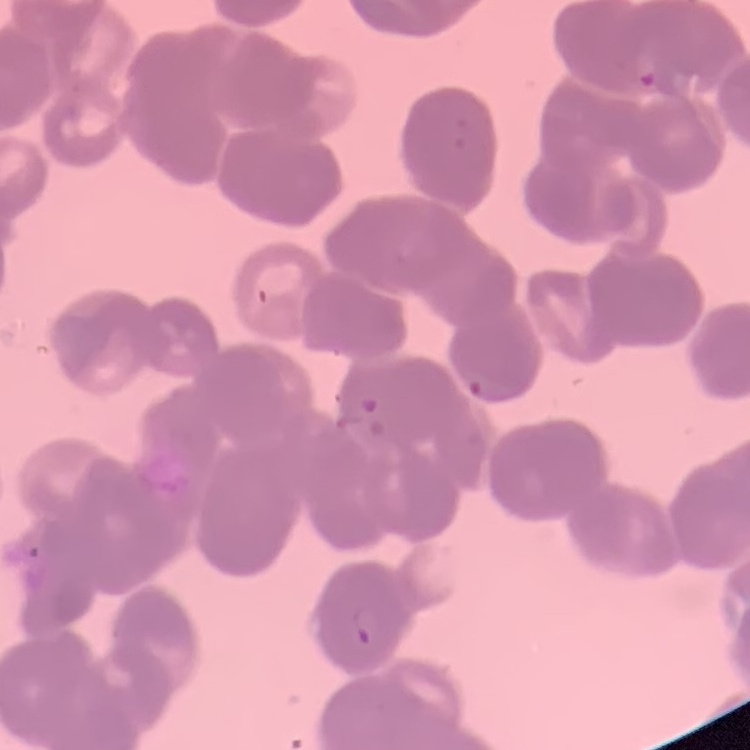
The red blood cells exhibit rouleaux formation. Square crop of a larger photomicrograph. Field's or Giemsa stain. Thin blood film.